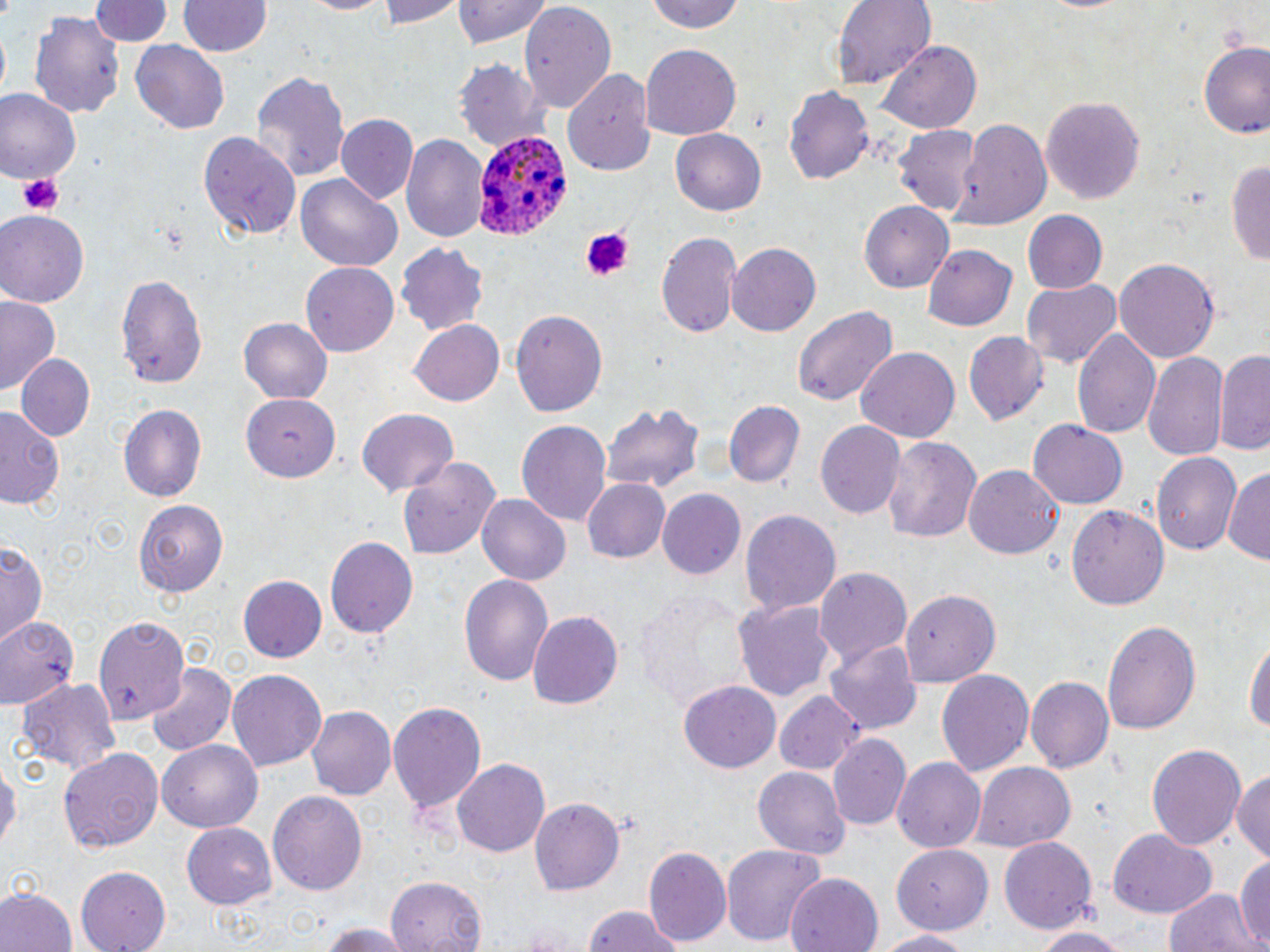
Approximate bounding boxes as (x1, y1, x2, y2) in pixels. Platelet locations: (18, 172, 63, 217), (577, 227, 636, 283). Uninfected red blood cell locations: (296, 0, 393, 15), (379, 0, 463, 28), (453, 0, 550, 49), (645, 0, 750, 35), (833, 0, 935, 89), (93, 1, 169, 49), (178, 2, 271, 58), (517, 4, 614, 114), (31, 10, 123, 118), (131, 41, 229, 133), (881, 41, 978, 133), (1199, 41, 1270, 142), (642, 45, 739, 140), (455, 57, 546, 153), (563, 68, 654, 175), (252, 71, 349, 184), (786, 84, 874, 187), (0, 92, 79, 183), (1040, 95, 1144, 205), (334, 115, 416, 204), (950, 120, 1052, 230), (892, 126, 980, 216), (672, 130, 765, 216), (200, 131, 297, 242), (402, 134, 487, 244), (1228, 158, 1270, 270), (295, 173, 401, 272), (860, 200, 954, 292), (1023, 210, 1108, 295), (0, 211, 89, 308), (656, 232, 742, 339), (396, 240, 488, 338), (727, 243, 820, 337), (921, 246, 1018, 333), (1115, 258, 1220, 365), (300, 263, 399, 358), (114, 269, 208, 390), (1020, 279, 1121, 368), (0, 298, 60, 395), (794, 303, 898, 409), (511, 308, 609, 417), (238, 319, 332, 406), (408, 320, 503, 407), (1073, 326, 1162, 441), (963, 329, 1050, 424), (856, 346, 960, 443), (1214, 348, 1270, 456), (1143, 351, 1228, 466), (15, 352, 95, 441), (244, 395, 341, 482), (723, 400, 804, 488), (119, 404, 207, 501), (603, 404, 705, 494), (0, 406, 65, 512), (356, 409, 458, 497), (517, 420, 611, 528), (1027, 420, 1127, 510), (817, 422, 905, 521), (880, 434, 981, 546), (1152, 451, 1242, 558), (396, 455, 500, 560), (965, 463, 1065, 559), (1223, 467, 1270, 567), (581, 478, 671, 564), (658, 490, 745, 580), (477, 494, 571, 586), (135, 498, 229, 597), (1066, 502, 1169, 608), (740, 509, 843, 618), (325, 534, 418, 637), (0, 541, 46, 647), (814, 566, 912, 667), (459, 573, 554, 689), (240, 576, 327, 662), (635, 588, 748, 709), (900, 589, 1000, 684), (733, 598, 835, 704), (529, 611, 623, 711), (0, 614, 87, 711), (96, 616, 192, 722), (1102, 617, 1200, 738), (1246, 629, 1269, 740), (826, 640, 919, 735), (146, 663, 237, 754), (228, 670, 326, 771), (936, 670, 1037, 776), (1026, 676, 1114, 775), (17, 678, 122, 775), (678, 678, 781, 773), (774, 687, 864, 775), (387, 700, 485, 815), (309, 705, 399, 799), (829, 732, 908, 832), (159, 739, 263, 831), (1146, 742, 1247, 852), (58, 746, 163, 852), (0, 756, 18, 857), (451, 759, 550, 857), (893, 759, 985, 851), (974, 763, 1074, 852), (751, 766, 849, 858), (1232, 768, 1270, 870), (267, 790, 368, 895), (528, 796, 626, 895), (182, 824, 274, 909), (1107, 830, 1215, 916), (998, 836, 1097, 934), (721, 843, 827, 945), (887, 845, 995, 937), (645, 846, 731, 949), (1232, 852, 1270, 950), (74, 867, 171, 952), (786, 874, 881, 952), (384, 875, 486, 952), (1164, 886, 1259, 952), (0, 888, 75, 952), (578, 906, 690, 952), (316, 923, 417, 952), (1031, 925, 1129, 952), (875, 928, 979, 951). Plasmodium ovale-infected red blood cell locations: (470, 128, 572, 241). Slide-level diagnosis: Plasmodium ovale. One field of a larger specimen. Image is 1270×952 pixels. May-Grünwald-Giemsa-stained preparation. Captured at 1000x magnification. Optical microscopy. Thin blood film.